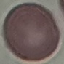
Summary:
  - Result: no malaria parasites seen
  - Preparation: thin blood smear
  - Capture: smartphone camera at the microscope eyepiece
  - Stain: Giemsa
  - Image type: automatically extracted cell patch, resized to 64 × 64 pixels